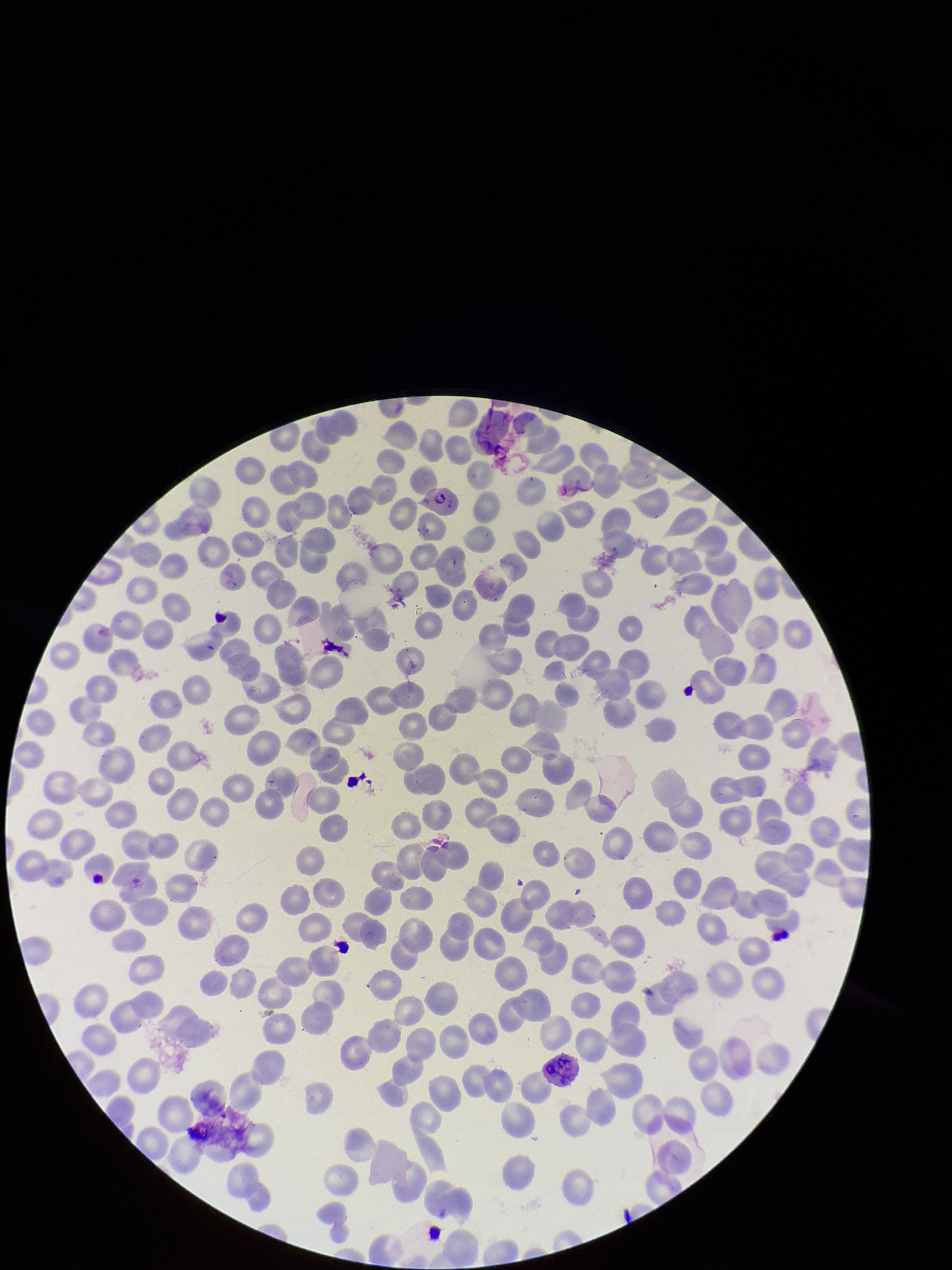

Species reported for this patient: Plasmodium falciparum. Parasitized red blood cells: identified. Giemsa stain. One field from this slide. Parasitized red blood cell count: 1. Image is 952×1270 pixels. Red blood cell count: 298. Preparation: thin blood smear. Patient malaria status: infected. Photographed through the microscope eyepiece with a smartphone camera.